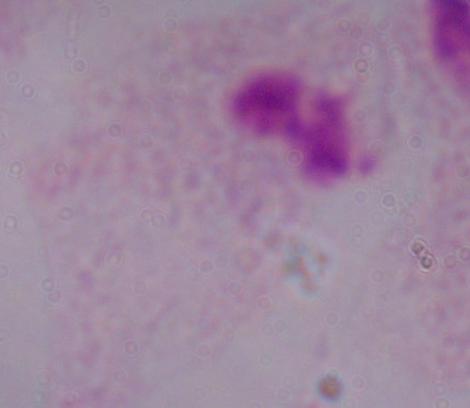
A trichomonad is seen. Micrograph. 1000x magnification.